Point out each Plasmodium parasite.
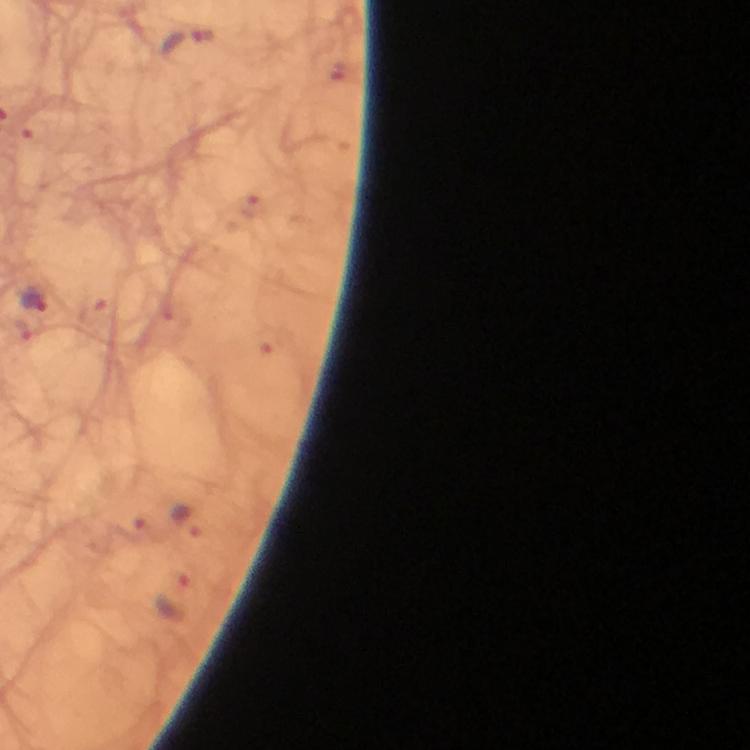

Approximate object centers, in pixels from the top-left corner.
Plasmodium parasites: (x=186, y=42), (x=35, y=299).

Summary:
  - Image size: 750×750 pixels
  - Preparation: thick smear
  - Cropped from: a single field of view
  - Stain: Giemsa
  - Context: from a malaria diagnostic workup
  - Immersion oil: applied
  - Magnification: 100x
  - Capture: smartphone mounted on the microscope